Locate every blood parasite and identify its species.
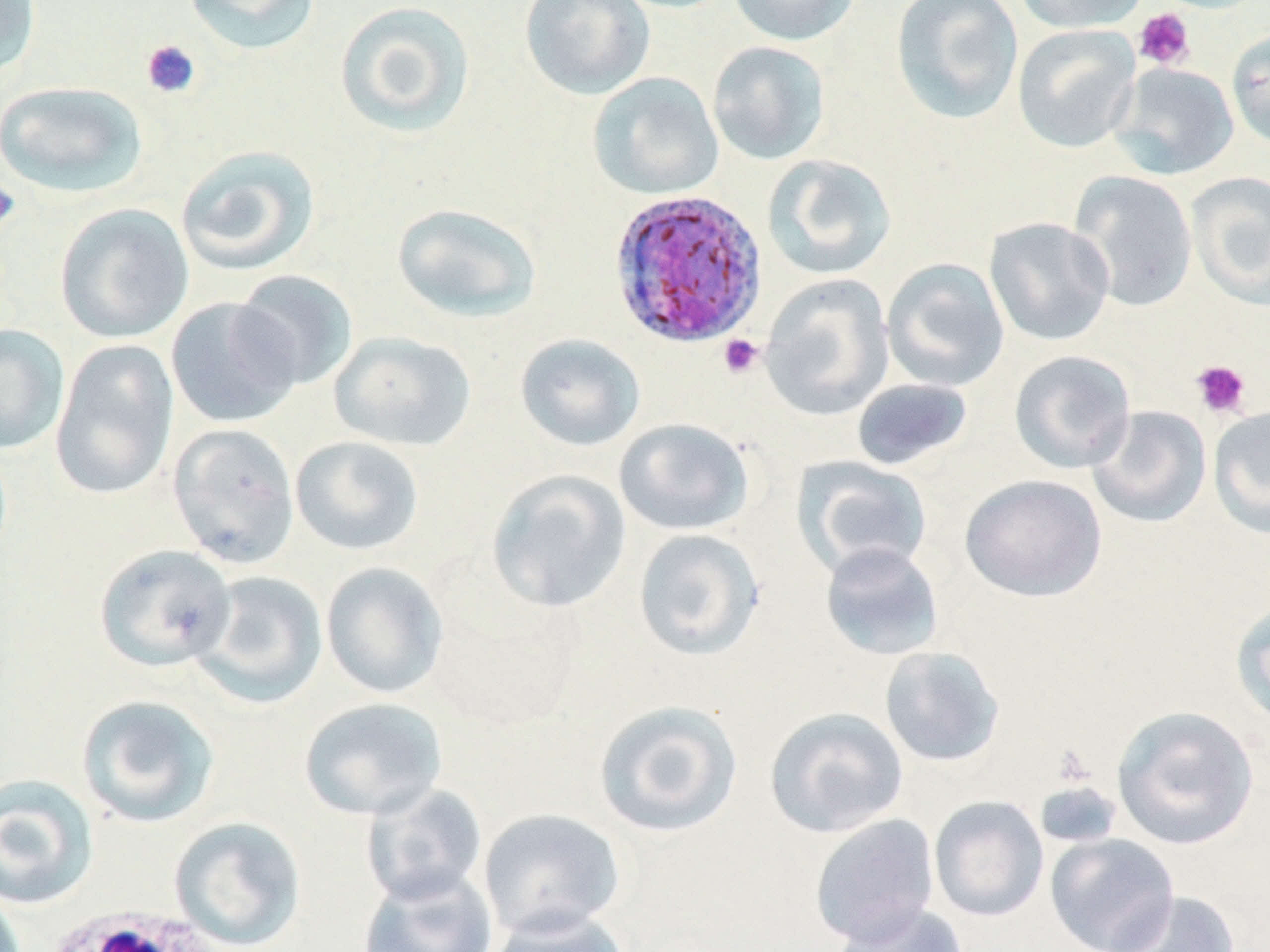
Approximate bounding boxes as named x1/y1/x2/y2 corners in pixels.
Plasmodium ovale-infected red blood cells: (x1=607, y1=188, x2=768, y2=349).
No Plasmodium falciparum, Plasmodium malariae, Plasmodium vivax, Babesia divergens, or Trypanosoma brucei observed.

Summary:
  - Uninfected red blood cell locations: (x1=0, y1=0, x2=41, y2=81), (x1=183, y1=0, x2=320, y2=55), (x1=334, y1=0, x2=477, y2=138), (x1=519, y1=0, x2=655, y2=101), (x1=727, y1=0, x2=861, y2=46), (x1=890, y1=0, x2=1024, y2=124), (x1=1014, y1=0, x2=1149, y2=34), (x1=1012, y1=23, x2=1141, y2=154), (x1=1226, y1=29, x2=1270, y2=151), (x1=707, y1=40, x2=831, y2=166), (x1=1109, y1=63, x2=1239, y2=180), (x1=588, y1=72, x2=724, y2=201), (x1=0, y1=80, x2=148, y2=198), (x1=175, y1=145, x2=320, y2=276), (x1=762, y1=154, x2=897, y2=280), (x1=1069, y1=171, x2=1197, y2=312), (x1=1185, y1=171, x2=1270, y2=311), (x1=391, y1=202, x2=543, y2=324), (x1=54, y1=203, x2=193, y2=344), (x1=984, y1=216, x2=1115, y2=347), (x1=881, y1=258, x2=1009, y2=393), (x1=232, y1=269, x2=359, y2=391), (x1=759, y1=274, x2=895, y2=420), (x1=165, y1=297, x2=302, y2=429), (x1=0, y1=324, x2=69, y2=455), (x1=329, y1=331, x2=477, y2=452), (x1=514, y1=333, x2=646, y2=452), (x1=49, y1=338, x2=179, y2=501), (x1=1009, y1=349, x2=1136, y2=474), (x1=850, y1=377, x2=973, y2=471), (x1=1087, y1=405, x2=1212, y2=528), (x1=1208, y1=405, x2=1270, y2=538), (x1=613, y1=418, x2=755, y2=536), (x1=167, y1=423, x2=301, y2=569), (x1=290, y1=435, x2=424, y2=556), (x1=795, y1=457, x2=934, y2=579), (x1=486, y1=469, x2=632, y2=613), (x1=960, y1=474, x2=1107, y2=602), (x1=632, y1=528, x2=766, y2=661), (x1=819, y1=542, x2=944, y2=661), (x1=94, y1=543, x2=235, y2=672), (x1=320, y1=562, x2=448, y2=699), (x1=193, y1=570, x2=328, y2=708), (x1=1230, y1=596, x2=1270, y2=728), (x1=879, y1=646, x2=1006, y2=768), (x1=76, y1=694, x2=221, y2=828), (x1=298, y1=696, x2=447, y2=820), (x1=592, y1=699, x2=744, y2=838), (x1=1112, y1=705, x2=1259, y2=850), (x1=764, y1=706, x2=908, y2=838), (x1=0, y1=774, x2=99, y2=910), (x1=1034, y1=781, x2=1122, y2=850), (x1=360, y1=783, x2=488, y2=907), (x1=928, y1=795, x2=1049, y2=922), (x1=477, y1=808, x2=626, y2=940), (x1=808, y1=813, x2=940, y2=948), (x1=168, y1=816, x2=307, y2=950), (x1=1045, y1=833, x2=1179, y2=951), (x1=356, y1=868, x2=498, y2=952), (x1=1102, y1=891, x2=1241, y2=952), (x1=829, y1=902, x2=970, y2=952), (x1=485, y1=907, x2=631, y2=952)
  - Platelet locations: (x1=1132, y1=8, x2=1195, y2=71), (x1=140, y1=39, x2=202, y2=99), (x1=0, y1=178, x2=21, y2=234), (x1=718, y1=334, x2=763, y2=379), (x1=1191, y1=359, x2=1251, y2=419), (x1=1051, y1=744, x2=1096, y2=788)
  - White blood cell locations: (x1=40, y1=907, x2=225, y2=952)
  - Slide-level diagnosis: Plasmodium ovale
  - Image size: 1270×952 pixels
  - Preparation: thin blood film
  - Modality: optical microscopy
  - Magnification: 1000x
  - Field of view: single
  - Stain: May-Grünwald-Giemsa